Report the malaria status of this cell.
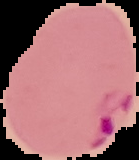

It is parasitized.

image_size: 139×160 pixels
image_type: segmented cell region on a black background
preparation: thin blood film